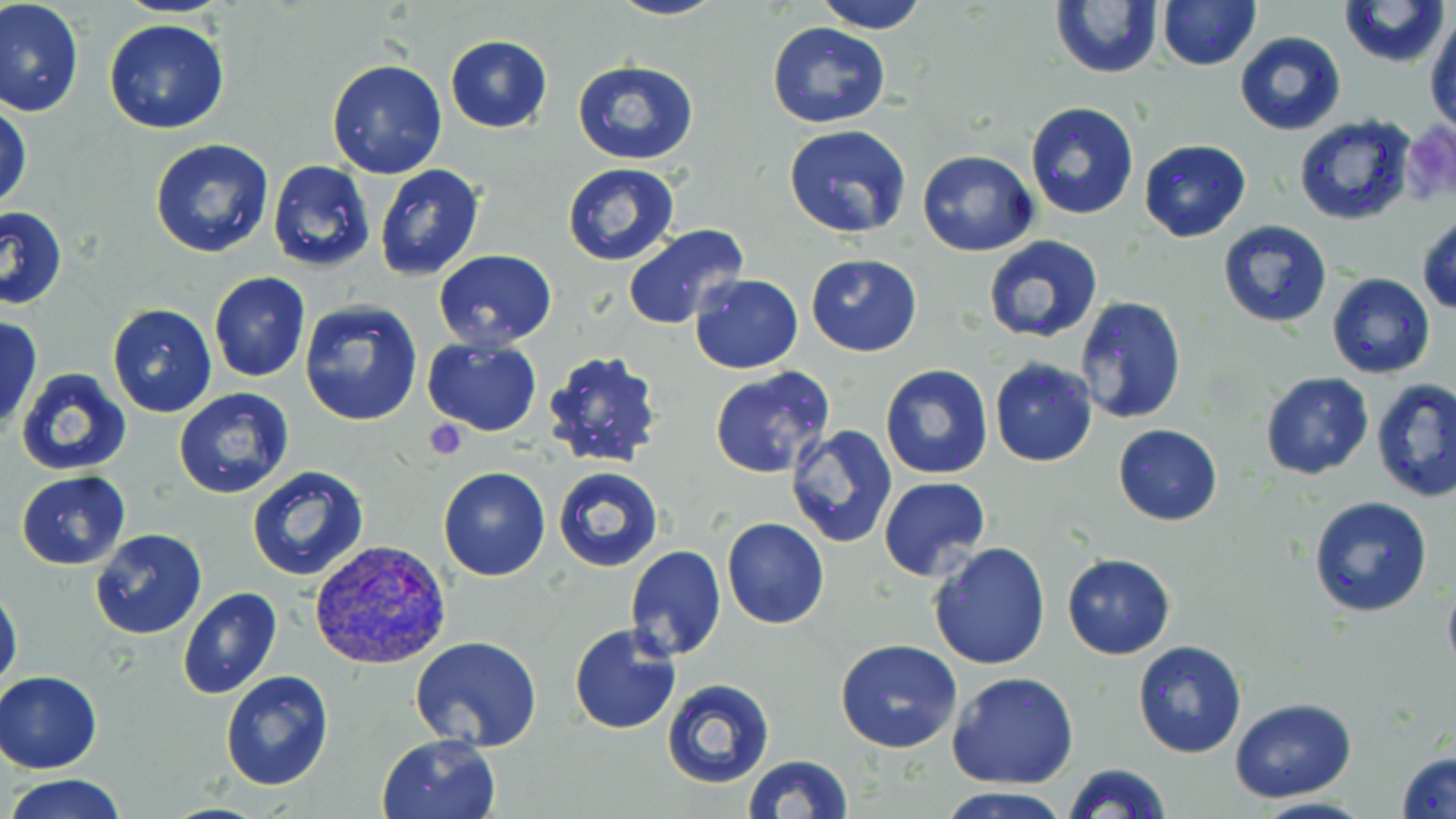
Summary:
  - Coordinate format: approximate bounding boxes as [x1, y1, x2, y2] in pixels
  - Plasmodium vivax-infected red blood cell locations: [310, 537, 451, 671]
  - Platelet locations: [1402, 119, 1456, 208], [424, 420, 469, 461]
  - Uninfected red blood cell locations: [605, 0, 728, 21], [816, 0, 928, 33], [1339, 0, 1450, 69], [0, 1, 84, 117], [1157, 1, 1260, 71], [1049, 2, 1162, 78], [1426, 13, 1456, 132], [104, 19, 231, 135], [766, 21, 891, 129], [1235, 31, 1346, 134], [445, 35, 552, 132], [326, 59, 448, 180], [573, 59, 699, 166], [0, 101, 31, 215], [1024, 101, 1139, 220], [1294, 116, 1417, 225], [784, 124, 912, 238], [149, 138, 276, 259], [1139, 139, 1251, 241], [917, 150, 1037, 257], [267, 160, 375, 272], [563, 163, 679, 266], [372, 164, 484, 281], [1, 206, 67, 310], [1417, 213, 1456, 313], [1217, 220, 1332, 329], [622, 223, 752, 330], [982, 236, 1104, 344], [432, 250, 558, 350], [806, 253, 923, 356], [208, 271, 312, 382], [1326, 272, 1435, 378], [690, 274, 803, 374], [1075, 295, 1188, 427], [298, 298, 423, 428], [106, 304, 218, 418], [0, 314, 43, 434], [422, 337, 544, 435], [540, 348, 667, 472], [988, 357, 1097, 467], [880, 363, 993, 479], [708, 366, 834, 478], [15, 368, 131, 476], [1260, 372, 1373, 479], [1371, 377, 1456, 502], [741, 384, 869, 530], [172, 388, 295, 498], [1114, 424, 1223, 525], [786, 425, 897, 549], [246, 464, 370, 582], [438, 466, 550, 581], [552, 466, 664, 573], [16, 471, 132, 569], [877, 476, 990, 580], [1308, 496, 1434, 619], [721, 518, 829, 630], [90, 529, 206, 640], [929, 542, 1051, 668], [625, 545, 727, 662], [1061, 554, 1175, 659], [1441, 575, 1456, 679], [0, 585, 23, 695], [176, 587, 281, 699], [568, 625, 681, 734], [409, 637, 543, 753], [835, 639, 963, 753], [1132, 639, 1247, 759], [0, 670, 102, 774], [220, 670, 335, 791], [946, 673, 1078, 789], [661, 679, 774, 787], [1230, 697, 1358, 803], [376, 732, 502, 819], [1396, 748, 1456, 819], [743, 755, 852, 818], [1062, 763, 1171, 819], [7, 774, 128, 818], [938, 788, 1074, 819], [1245, 796, 1377, 819]
  - Slide-level diagnosis: Plasmodium vivax
  - Magnification: 1000x
  - Image size: 1456×819 pixels
  - Field of view: single
  - Preparation: thin blood film
  - Modality: optical microscopy
  - Stain: May-Grünwald-Giemsa